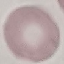

result: no malaria parasites seen
image_type: automatically extracted cell patch, resized to 64 × 64 pixels
capture: smartphone through the microscope eyepiece
preparation: thin blood film
stain: Giemsa